Describe the morphology of the red blood cells.
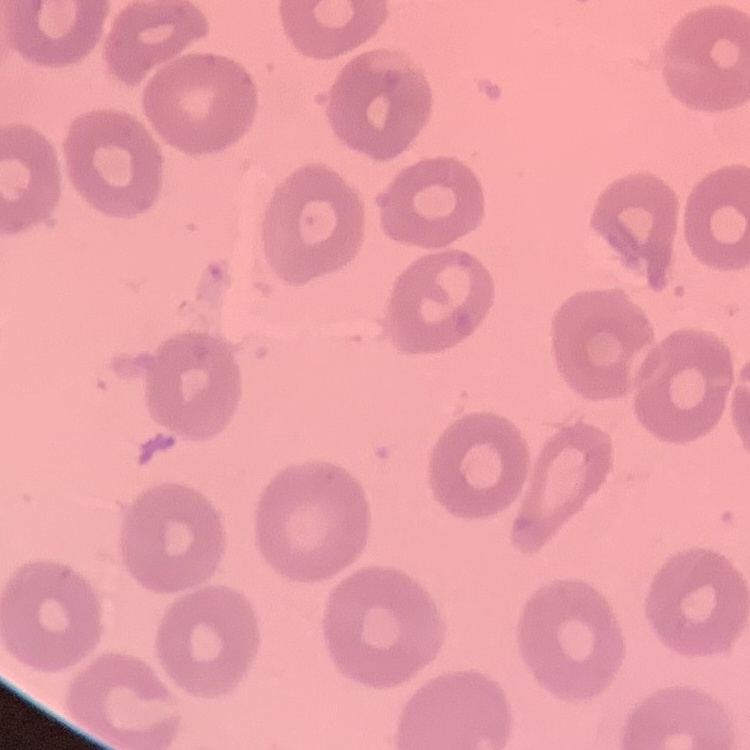

They show no rouleaux formation.

{
  "stain": "Field's or Giemsa",
  "image_type": "one tile cut from a larger photomicrograph",
  "preparation": "thin blood film"
}